Classify this cell by malaria status.
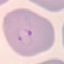

Parasitized.

Summary:
  - Preparation: thin blood film
  - Stain: Giemsa
  - Image type: cell patch, automatically extracted from a larger field of view and resized to 64 × 64 pixels
  - Capture: smartphone through the microscope eyepiece